State which parasite is depicted.
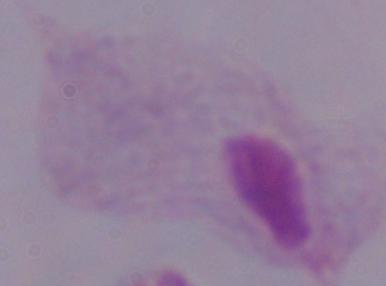
This is a trichomonad.

Summary:
  - Modality: micrograph
  - Magnification: 1000x